Identify the parasite.
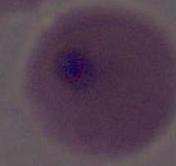

Plasmodium.

400x or 1000x magnification. Photomicrograph.